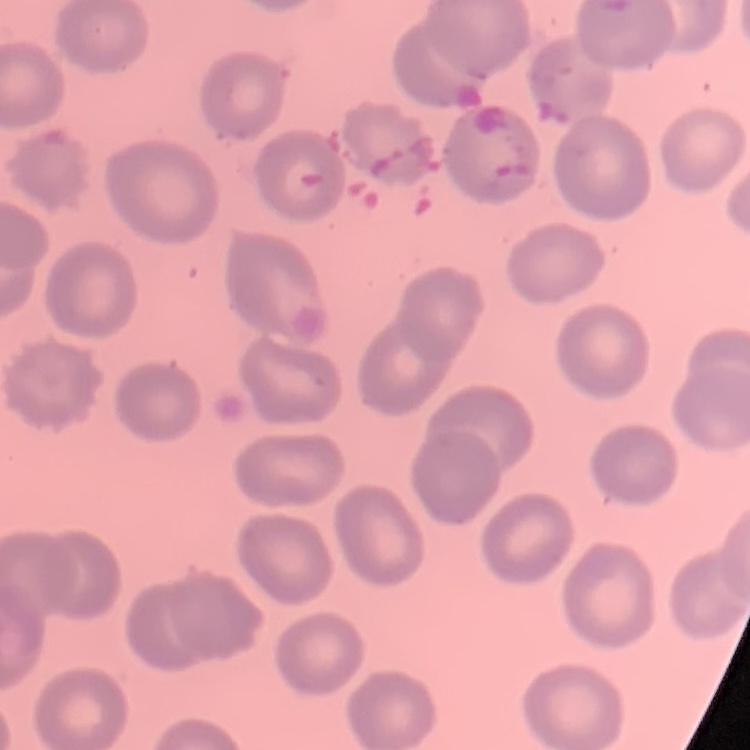

Summary:
  - Red blood cell morphology: no rouleaux formation
  - Image type: square crop of a larger photomicrograph
  - Preparation: thin blood film
  - Stain: Field's or Giemsa